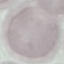 Malaria status: uninfected. Automatically extracted cell patch, resized to 64 × 64 pixels. Photographed with a smartphone camera at the microscope eyepiece. Giemsa stain. Thin blood smear.